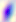
Photomicrograph. 400x magnification. Toxoplasma gondii is seen.